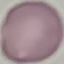

malaria status = uninfected
image type = automatically extracted cell patch, resized to 64 × 64 pixels
capture = smartphone through the microscope eyepiece
preparation = thin blood film
stain = Giemsa